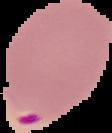

Summary:
  - Image size: 112×133 pixels
  - Preparation: thin blood smear
  - Malaria status: parasitized
  - Image type: segmented cell region with the area outside set to black